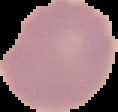
Summary:
  - Result: no Plasmodium parasites detected
  - Image size: 118×112 pixels
  - Image type: segmented cell region on a black background
  - Preparation: thin blood smear